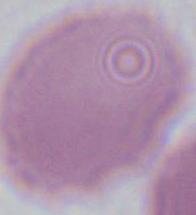

identification = red blood cell
modality = micrograph
magnification = 1000x